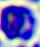
Micrograph. A leukocyte is seen. 400x magnification.